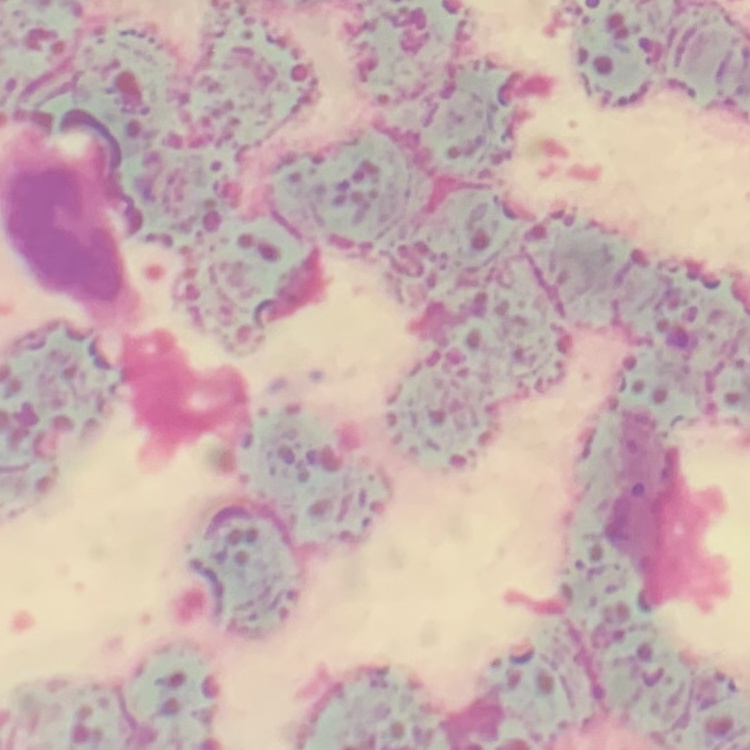

Summary:
  - Red blood cell morphology: rouleaux formation
  - Stain: Field's or Giemsa
  - Image type: square crop of a larger photomicrograph
  - Preparation: thin blood film